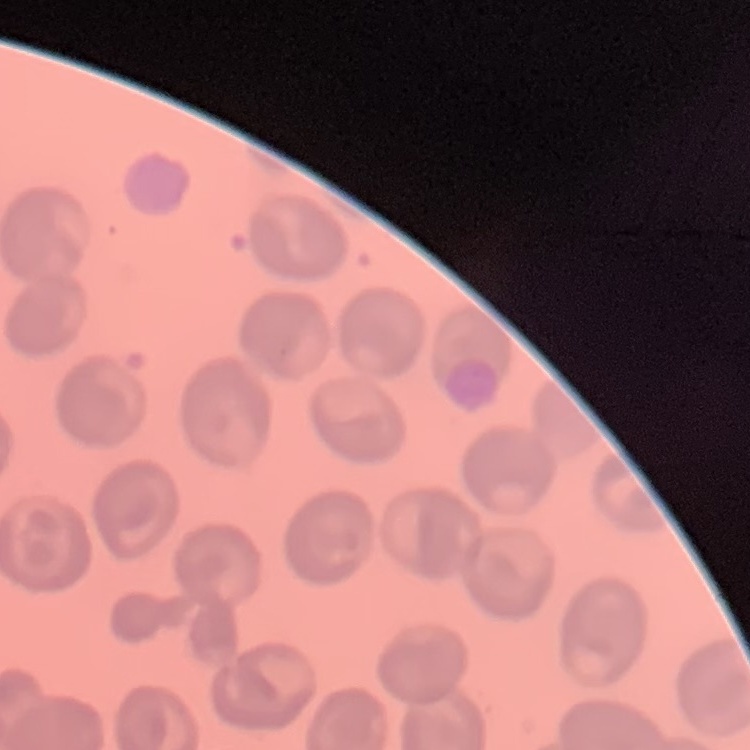
erythrocyte_morphology: no rouleaux formation
preparation: thin blood film
stain: Field's or Giemsa
image_type: square crop of a larger photomicrograph